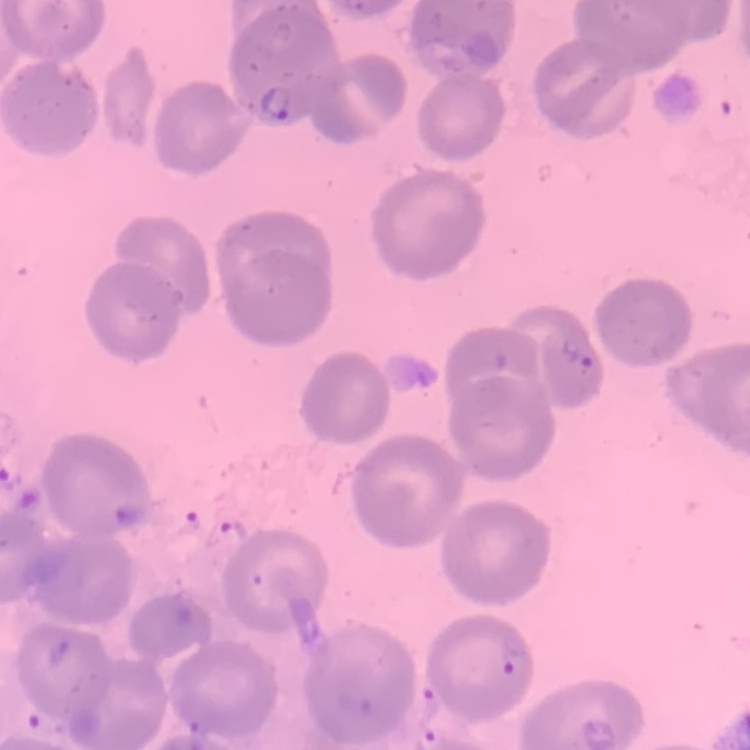
red blood cell morphology = no rouleaux formation
stain = Field's or Giemsa
image type = square crop of a larger photomicrograph
preparation = thin blood smear